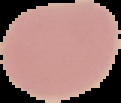

image size = 121×103 pixels
malaria status = uninfected
image type = segmented cell region with the area outside set to black
preparation = thin blood film